Assess the morphology of the red blood cells.
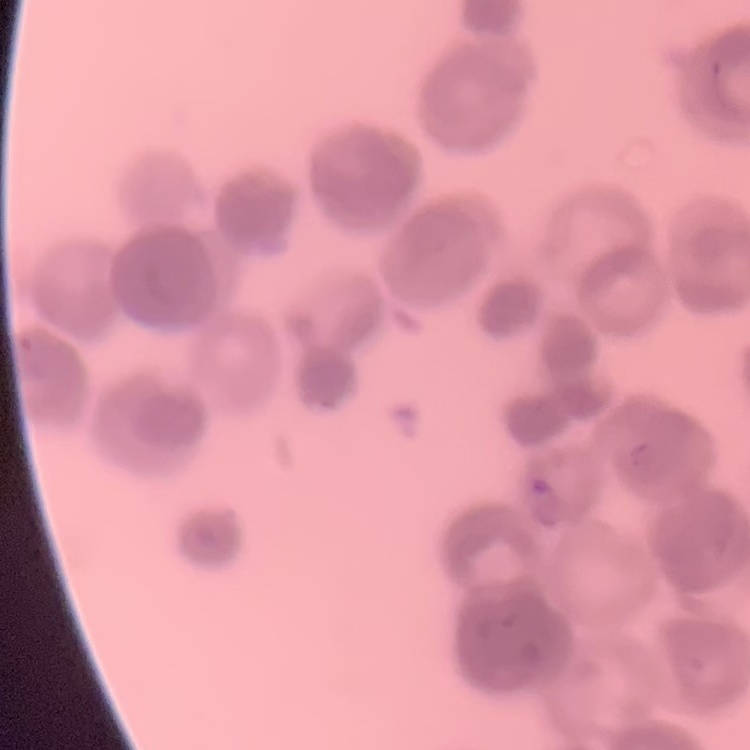
They show rouleaux formation.

Field's or Giemsa stain. One tile cut from a larger photomicrograph. Thin blood film.